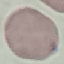 Result: no malaria parasites seen. Giemsa-stained preparation. Photographed with a smartphone camera at the microscope eyepiece. Automatically extracted cell patch, resized to 64 × 64 pixels. Thin blood smear.